Mark where platelets are.
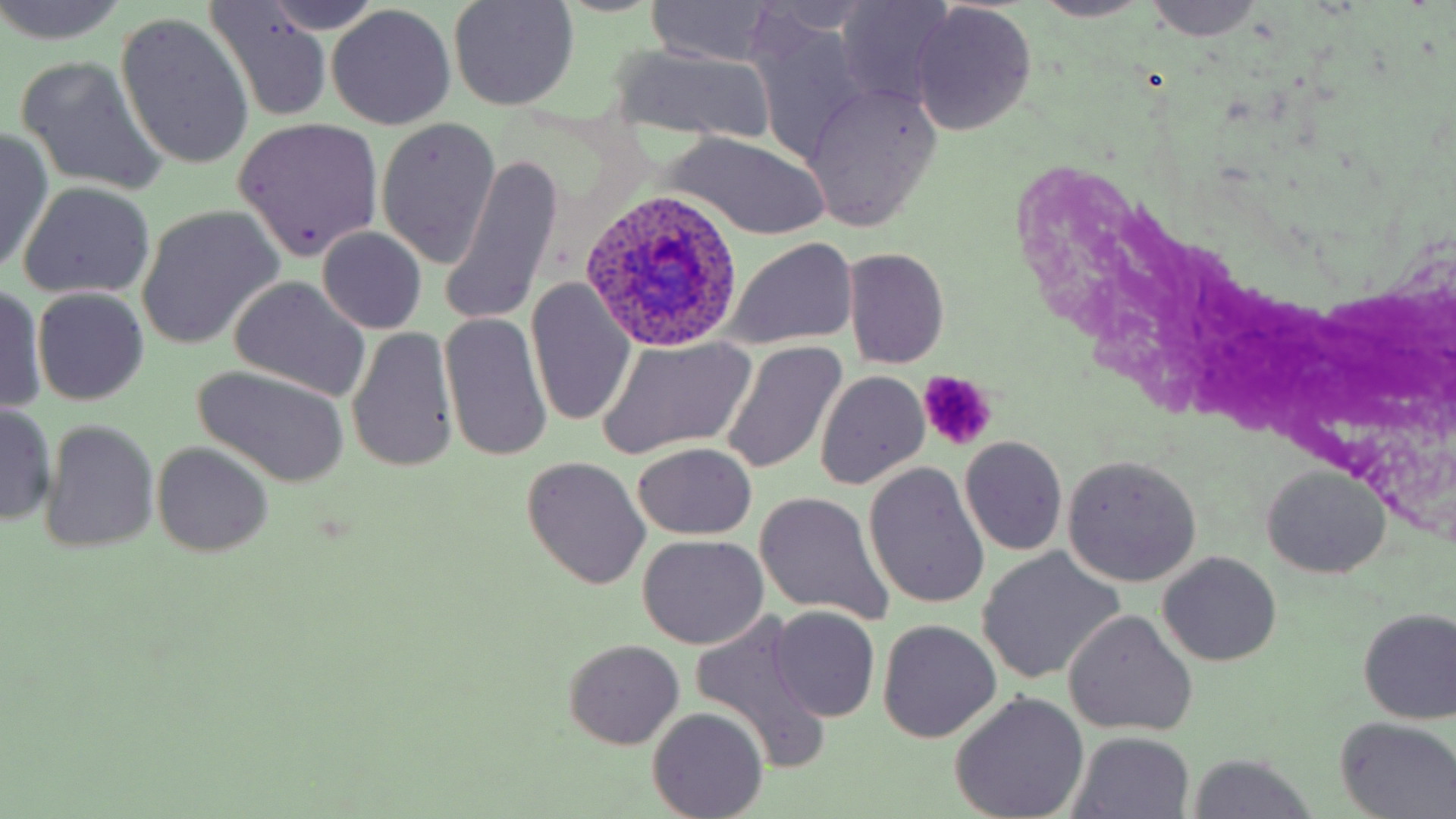
Approximate bounding boxes as named x1/y1/x2/y2 corners in pixels.
Platelets: (x1=916, y1=370, x2=996, y2=448).

{
  "slide_level_diagnosis": "Plasmodium ovale",
  "modality": "light microscopy",
  "image_size": "1456×819 pixels",
  "uninfected_red_blood_cell_locations": "approximate bounding boxes as named x1/y1/x2/y2 corners in pixels: (x1=0, y1=0, x2=131, y2=47), (x1=447, y1=0, x2=579, y2=111), (x1=1031, y1=0, x2=1153, y2=22), (x1=1144, y1=0, x2=1261, y2=40), (x1=647, y1=1, x2=779, y2=68), (x1=834, y1=1, x2=960, y2=108), (x1=206, y1=4, x2=335, y2=118), (x1=908, y1=5, x2=1036, y2=133), (x1=325, y1=7, x2=455, y2=129), (x1=116, y1=15, x2=254, y2=170), (x1=607, y1=43, x2=779, y2=147), (x1=16, y1=55, x2=165, y2=194), (x1=803, y1=85, x2=943, y2=229), (x1=231, y1=117, x2=383, y2=262), (x1=376, y1=118, x2=501, y2=268), (x1=0, y1=129, x2=52, y2=273), (x1=664, y1=133, x2=831, y2=239), (x1=440, y1=153, x2=562, y2=327), (x1=18, y1=182, x2=155, y2=300), (x1=138, y1=207, x2=282, y2=347), (x1=316, y1=227, x2=428, y2=335), (x1=724, y1=239, x2=858, y2=349), (x1=843, y1=247, x2=950, y2=368), (x1=228, y1=277, x2=371, y2=400), (x1=527, y1=278, x2=637, y2=429), (x1=0, y1=281, x2=46, y2=415), (x1=33, y1=289, x2=150, y2=405), (x1=439, y1=311, x2=553, y2=463), (x1=347, y1=326, x2=460, y2=473), (x1=595, y1=337, x2=756, y2=459), (x1=720, y1=341, x2=848, y2=476), (x1=189, y1=368, x2=350, y2=488), (x1=815, y1=371, x2=930, y2=490), (x1=1, y1=400, x2=57, y2=526), (x1=41, y1=420, x2=159, y2=554), (x1=959, y1=436, x2=1067, y2=556), (x1=153, y1=442, x2=273, y2=556), (x1=632, y1=442, x2=756, y2=539), (x1=1063, y1=455, x2=1203, y2=586), (x1=521, y1=459, x2=651, y2=591), (x1=864, y1=462, x2=990, y2=610), (x1=1260, y1=466, x2=1391, y2=580), (x1=755, y1=492, x2=891, y2=623), (x1=636, y1=535, x2=770, y2=650), (x1=977, y1=549, x2=1124, y2=683), (x1=1159, y1=552, x2=1281, y2=667), (x1=768, y1=607, x2=880, y2=723), (x1=1358, y1=608, x2=1456, y2=725), (x1=1064, y1=612, x2=1197, y2=737), (x1=691, y1=614, x2=831, y2=771), (x1=878, y1=620, x2=1002, y2=742), (x1=563, y1=639, x2=685, y2=749), (x1=951, y1=693, x2=1088, y2=819), (x1=649, y1=708, x2=767, y2=819), (x1=1335, y1=717, x2=1456, y2=818), (x1=1070, y1=734, x2=1194, y2=819), (x1=1190, y1=756, x2=1314, y2=819)",
  "field_of_view": "single",
  "magnification": "1000x",
  "stain": "May-Grünwald-Giemsa",
  "preparation": "thin blood film",
  "plasmodium_ovale_infected_red_blood_cell_locations": "approximate bounding boxes as named x1/y1/x2/y2 corners in pixels: (x1=578, y1=190, x2=742, y2=352)"
}